Report the malaria status of this cell.
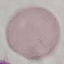
Uninfected.

Thin smear of blood. Automatically extracted cell patch, resized to 64 × 64 pixels. Acquired by smartphone through the microscope eyepiece. Giemsa stain.